Classify this cell by malaria status.
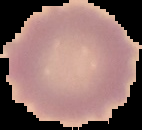

Uninfected.

preparation = thin blood film
image size = 142×130 pixels
image type = segmented cell region on a black background